Outline each Plasmodium falciparum-infected red blood cell.
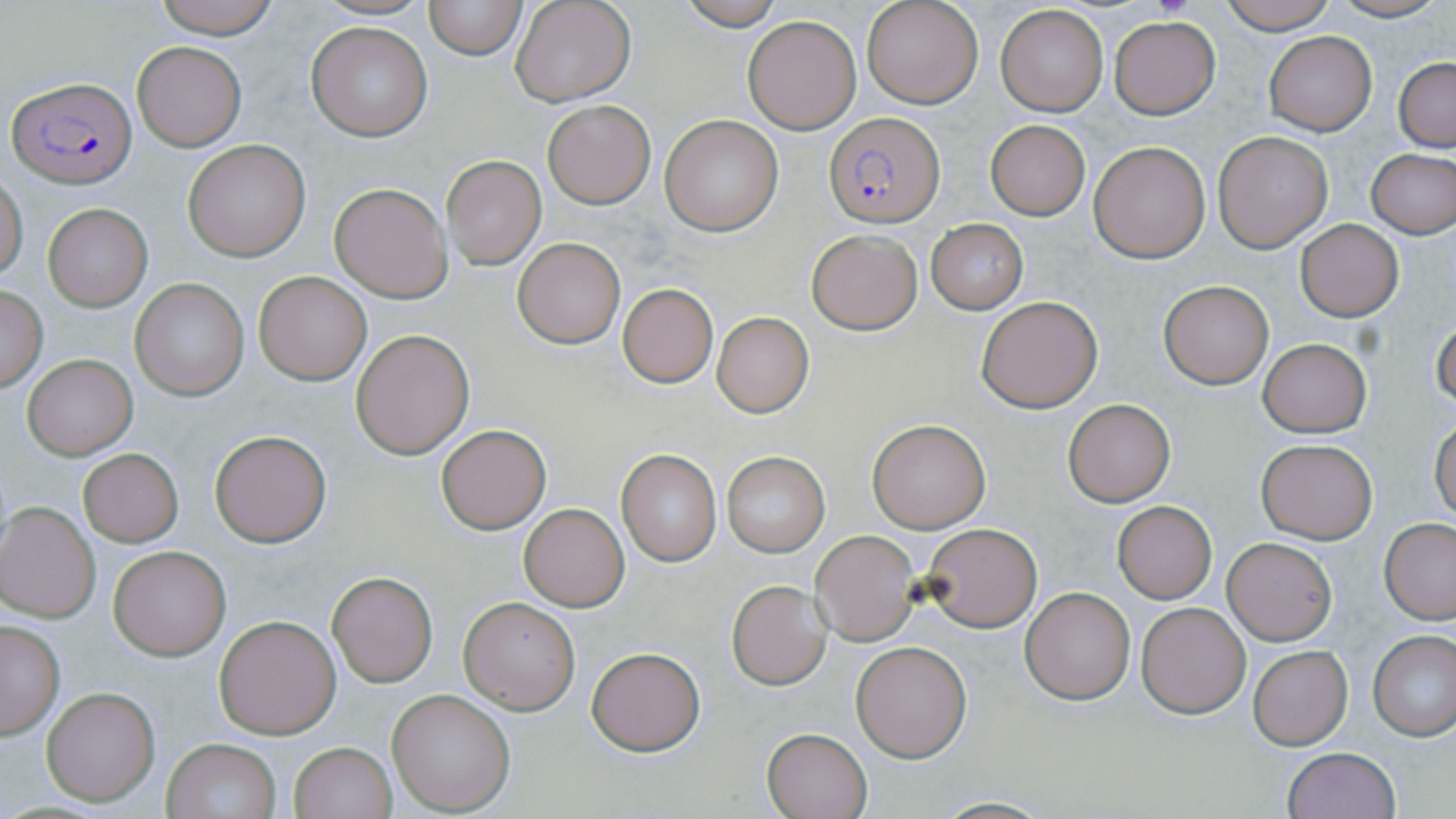

Approximate bounding boxes as named x1/y1/x2/y2 corners in pixels.
Plasmodium falciparum-infected red blood cells: (x1=7, y1=75, x2=136, y2=187), (x1=824, y1=112, x2=944, y2=227).

Uninfected red blood cell locations: (x1=151, y1=0, x2=283, y2=40), (x1=314, y1=0, x2=432, y2=22), (x1=424, y1=0, x2=528, y2=59), (x1=510, y1=0, x2=637, y2=106), (x1=678, y1=0, x2=787, y2=29), (x1=861, y1=0, x2=982, y2=109), (x1=1219, y1=0, x2=1339, y2=34), (x1=1326, y1=0, x2=1448, y2=24), (x1=996, y1=5, x2=1109, y2=116), (x1=742, y1=16, x2=862, y2=135), (x1=1109, y1=17, x2=1220, y2=118), (x1=307, y1=22, x2=432, y2=142), (x1=1263, y1=31, x2=1377, y2=135), (x1=132, y1=41, x2=246, y2=150), (x1=1394, y1=58, x2=1455, y2=152), (x1=542, y1=100, x2=655, y2=208), (x1=659, y1=116, x2=783, y2=236), (x1=984, y1=119, x2=1091, y2=220), (x1=1215, y1=131, x2=1332, y2=251), (x1=184, y1=139, x2=311, y2=261), (x1=1088, y1=140, x2=1212, y2=263), (x1=1365, y1=148, x2=1456, y2=238), (x1=442, y1=155, x2=545, y2=269), (x1=0, y1=174, x2=27, y2=279), (x1=328, y1=182, x2=452, y2=302), (x1=44, y1=204, x2=151, y2=312), (x1=925, y1=219, x2=1028, y2=314), (x1=1295, y1=219, x2=1404, y2=323), (x1=806, y1=229, x2=924, y2=334), (x1=513, y1=238, x2=625, y2=349), (x1=254, y1=272, x2=372, y2=385), (x1=130, y1=278, x2=248, y2=400), (x1=1158, y1=281, x2=1273, y2=389), (x1=617, y1=284, x2=718, y2=387), (x1=0, y1=287, x2=49, y2=391), (x1=977, y1=296, x2=1101, y2=412), (x1=711, y1=313, x2=815, y2=419), (x1=1431, y1=315, x2=1455, y2=411), (x1=349, y1=329, x2=474, y2=459), (x1=1258, y1=338, x2=1372, y2=438), (x1=23, y1=354, x2=137, y2=460), (x1=1062, y1=399, x2=1176, y2=506), (x1=867, y1=419, x2=991, y2=533), (x1=1430, y1=419, x2=1455, y2=524), (x1=436, y1=424, x2=551, y2=534), (x1=210, y1=429, x2=332, y2=547), (x1=1255, y1=438, x2=1378, y2=544), (x1=78, y1=449, x2=183, y2=547), (x1=617, y1=450, x2=721, y2=564), (x1=721, y1=452, x2=828, y2=556), (x1=0, y1=501, x2=101, y2=622), (x1=1112, y1=501, x2=1218, y2=603), (x1=518, y1=502, x2=631, y2=612), (x1=1379, y1=517, x2=1456, y2=624), (x1=922, y1=523, x2=1042, y2=634), (x1=811, y1=531, x2=920, y2=645), (x1=1223, y1=537, x2=1336, y2=645), (x1=107, y1=545, x2=232, y2=661), (x1=327, y1=571, x2=437, y2=686), (x1=726, y1=581, x2=832, y2=690), (x1=1021, y1=586, x2=1135, y2=705), (x1=457, y1=596, x2=580, y2=715), (x1=1137, y1=602, x2=1251, y2=718), (x1=214, y1=615, x2=342, y2=739), (x1=0, y1=620, x2=65, y2=739), (x1=1369, y1=630, x2=1456, y2=741), (x1=852, y1=642, x2=971, y2=761), (x1=1248, y1=645, x2=1353, y2=749), (x1=586, y1=646, x2=707, y2=756), (x1=41, y1=687, x2=160, y2=807), (x1=387, y1=690, x2=515, y2=815), (x1=762, y1=728, x2=872, y2=818), (x1=160, y1=737, x2=283, y2=819), (x1=289, y1=741, x2=396, y2=819), (x1=1280, y1=748, x2=1401, y2=819), (x1=929, y1=797, x2=1058, y2=817). Slide-level diagnosis: Plasmodium falciparum. One field of a larger specimen. Image is 1456×819 pixels. Light microscopy. May-Grünwald-Giemsa stain. Captured at 1000x magnification. Thin blood film.